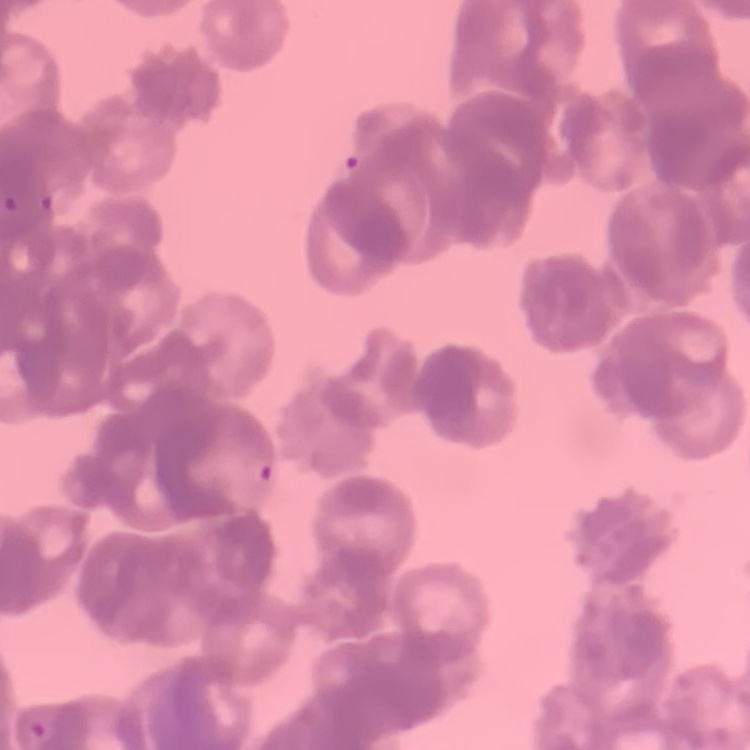
The red blood cells exhibit rouleaux formation. Thin peripheral smear. Stained with either Field's or Giemsa. One tile cut from a larger photomicrograph.